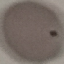

{
  "result": "negative for malaria parasites",
  "capture": "smartphone camera at the microscope eyepiece",
  "preparation": "thin blood film",
  "stain": "Giemsa",
  "image_type": "cell patch, automatically extracted from a larger field of view and resized to 64 × 64 pixels"
}